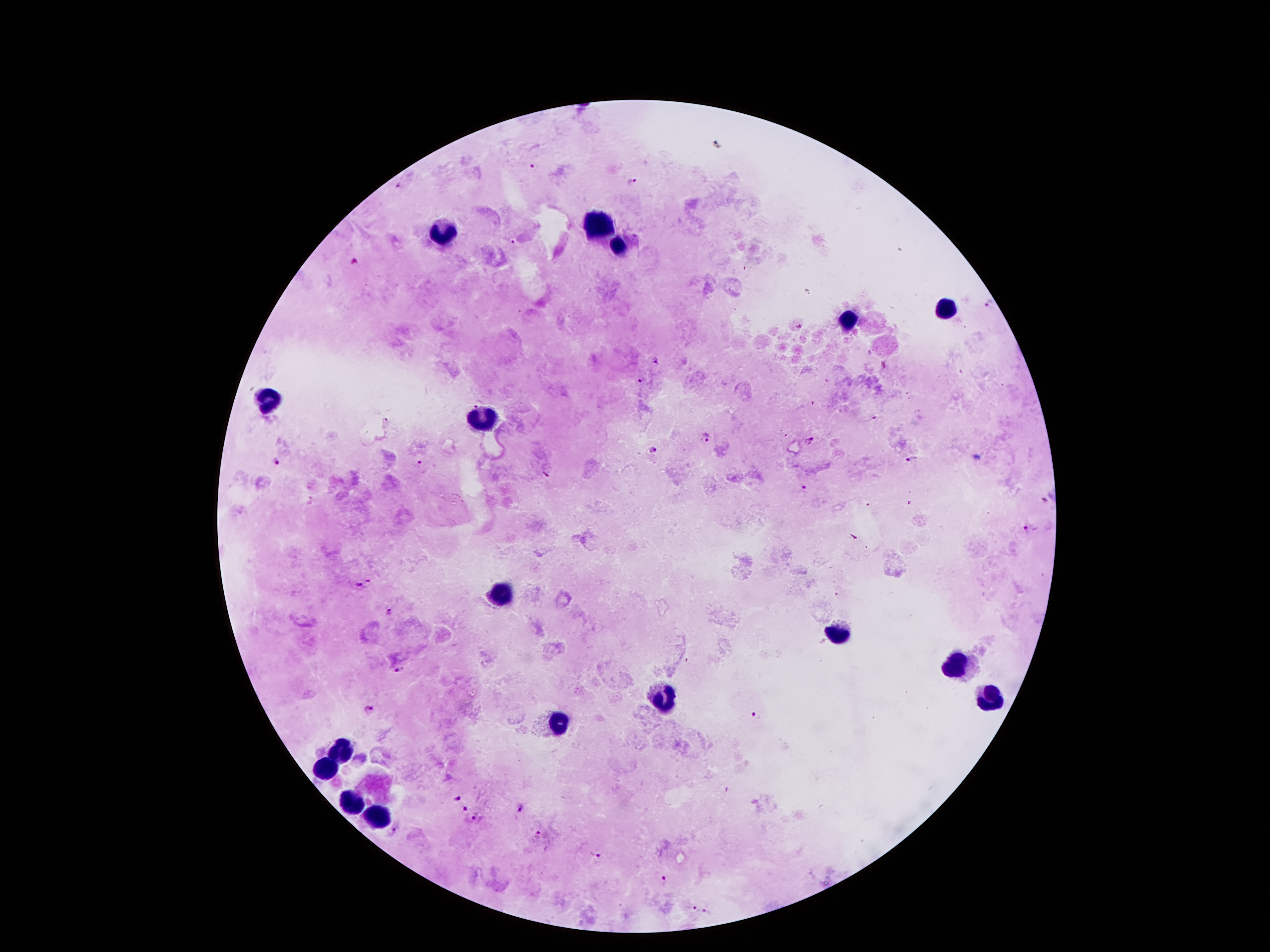

Approximate centers as [x, y] in pixels. Malaria parasite locations: [534, 167], [631, 179], [399, 185], [508, 241], [355, 260], [990, 302], [799, 327], [654, 362], [640, 382], [705, 435], [809, 442], [651, 450], [910, 459], [421, 460], [276, 462], [804, 488], [1047, 499], [1027, 530], [371, 581], [357, 585], [390, 612], [402, 669], [369, 711], [755, 716], [455, 798], [464, 807], [517, 809], [475, 816], [391, 829], [539, 835], [596, 855], [665, 882], [693, 909], [705, 913]. Leukocyte locations: [596, 225], [440, 232], [615, 246], [946, 309], [846, 321], [270, 400], [483, 414], [500, 592], [836, 632], [956, 668], [663, 700], [992, 702], [560, 721], [342, 752], [325, 769], [349, 803], [378, 815]. 100x magnification. Smartphone photograph taken through the microscope eyepiece. Thick peripheral-blood smear. Patient malaria status: positive for Plasmodium falciparum. Image is 1270×952 pixels. Single field of view. Giemsa-stained preparation.